State which parasite is depicted.
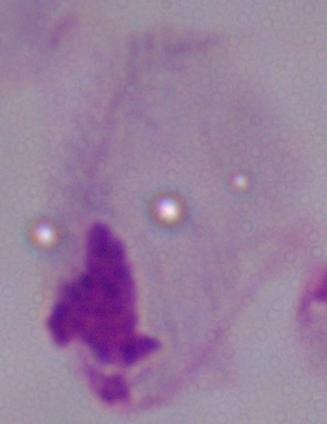

A trichomonad.

Summary:
  - Modality: micrograph
  - Magnification: 1000x